Outline each blood parasite and name the species.
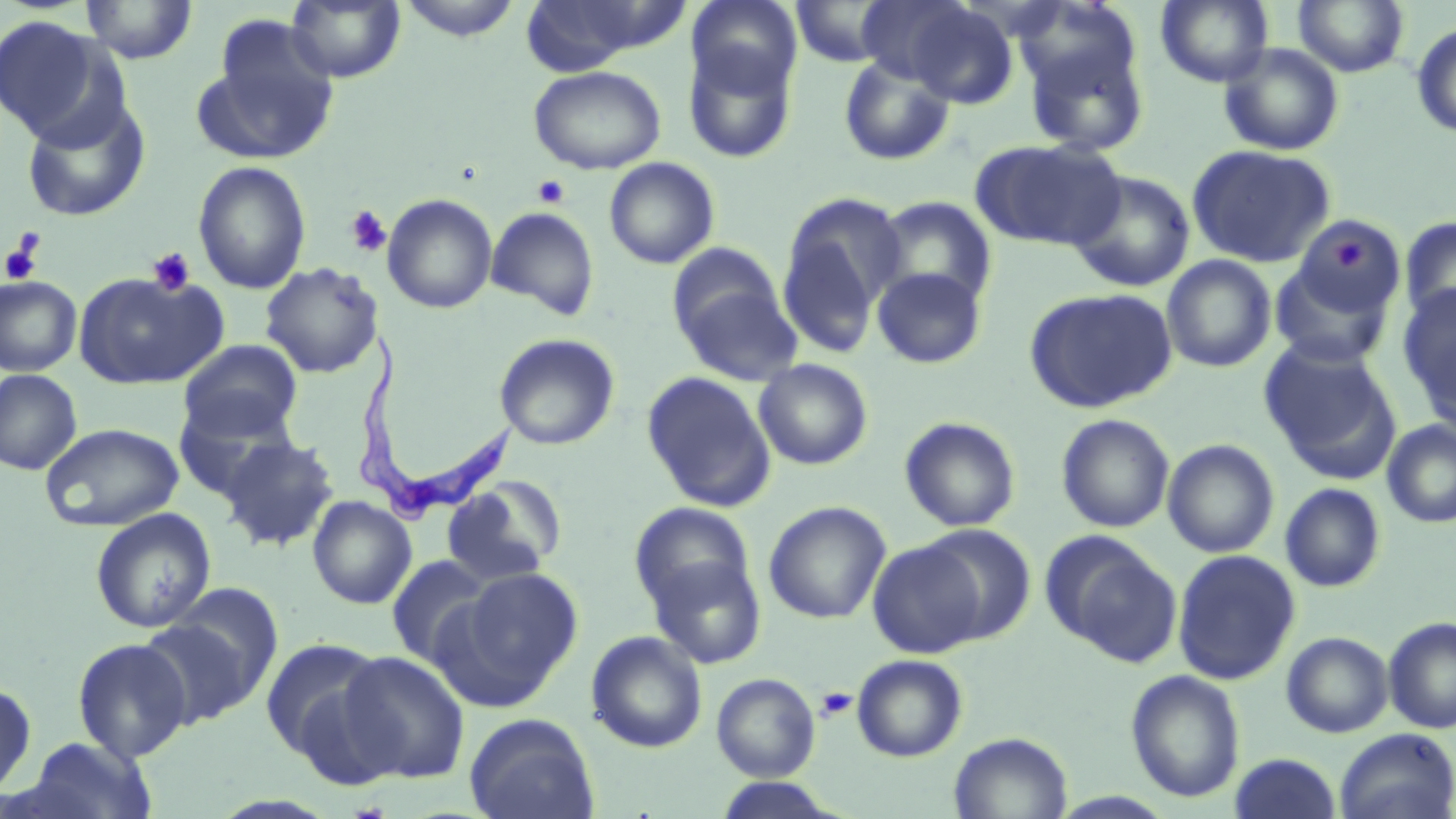

Approximate bounding boxes as (x1, y1, x2, y2) in pixels.
Trypanosoma brucei: (347, 329, 522, 524).
No Plasmodium falciparum, Plasmodium ovale, Plasmodium malariae, Plasmodium vivax, or Babesia divergens observed.

slide-level diagnosis = Trypanosoma brucei
uninfected red blood cell locations = approximate bounding boxes as (x1, y1, x2, y2) in pixels: (80, 0, 198, 64), (286, 0, 405, 83), (397, 0, 523, 42), (686, 0, 802, 97), (855, 0, 973, 84), (1155, 0, 1274, 87), (515, 1, 668, 74), (791, 1, 898, 68), (1293, 1, 1410, 77), (904, 3, 1019, 109), (0, 16, 107, 140), (203, 19, 340, 160), (1411, 23, 1456, 138), (1019, 30, 1151, 157), (682, 41, 799, 164), (1218, 43, 1345, 156), (837, 55, 956, 167), (528, 65, 666, 174), (21, 97, 150, 221), (971, 139, 1124, 251), (1187, 144, 1336, 267), (603, 156, 720, 269), (193, 160, 311, 294), (1066, 169, 1195, 293), (776, 192, 905, 356), (382, 193, 498, 314), (873, 196, 998, 309), (486, 206, 600, 321), (1293, 216, 1408, 321), (1400, 216, 1456, 325), (1161, 254, 1277, 373), (1268, 259, 1396, 368), (260, 262, 383, 378), (872, 266, 988, 370), (672, 268, 801, 387), (73, 271, 225, 390), (0, 276, 81, 377), (1398, 283, 1456, 415), (1024, 287, 1178, 414), (494, 333, 620, 450), (178, 339, 303, 441), (1259, 339, 1403, 484), (754, 359, 873, 470), (0, 369, 82, 476), (641, 371, 777, 513), (172, 395, 302, 504), (1056, 413, 1175, 533), (899, 416, 1021, 532), (1381, 419, 1456, 528), (39, 422, 185, 531), (219, 435, 339, 551), (1162, 439, 1279, 558), (440, 477, 565, 587), (1279, 483, 1386, 593), (307, 496, 416, 609), (763, 501, 892, 625), (629, 502, 757, 617), (90, 508, 215, 634), (916, 523, 1037, 644), (1041, 531, 1181, 666), (868, 539, 986, 658), (1172, 549, 1301, 685), (646, 552, 767, 670), (386, 555, 495, 670), (446, 567, 583, 702), (161, 581, 284, 706), (137, 615, 261, 728), (1382, 616, 1456, 733), (586, 630, 707, 753), (1281, 632, 1394, 738), (259, 635, 395, 774), (72, 637, 193, 762), (337, 650, 471, 785), (851, 654, 968, 762), (1125, 669, 1245, 803), (711, 672, 821, 781), (0, 681, 37, 800), (464, 713, 599, 819), (1334, 727, 1456, 819), (948, 732, 1073, 818), (23, 736, 157, 819), (1229, 753, 1344, 818), (711, 777, 844, 818)
platelet locations = approximate bounding boxes as (x1, y1, x2, y2) in pixels: (532, 175, 570, 209), (346, 204, 391, 257), (1330, 234, 1372, 274), (1, 235, 43, 286), (146, 247, 196, 296), (815, 687, 858, 722)
magnification = 1000x
stain = May-Grünwald-Giemsa
modality = optical microscopy
image size = 1456×819 pixels
field of view = single
preparation = thin blood smear